Identify the cell.
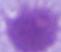
An erythrocyte.

Summary:
  - Magnification: 1000x
  - Modality: micrograph